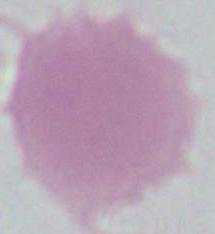
identification: erythrocyte
modality: micrograph
magnification: 1000x